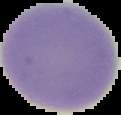
Summary:
  - Image type: segmented cell region on a black background
  - Preparation: thin blood smear
  - Image size: 121×115 pixels
  - Result: negative for malaria parasites